Identify the parasite.
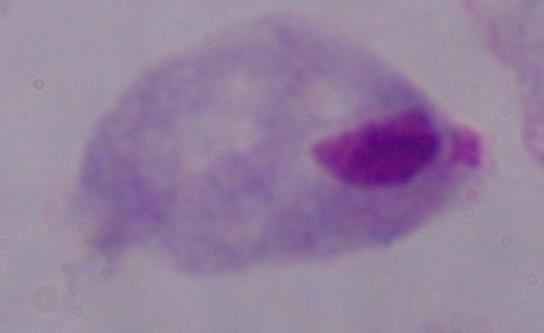

This is a trichomonad.

modality = micrograph
magnification = 1000x